Assess this cell for malaria.
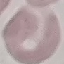

It is uninfected.

Summary:
  - Stain: Giemsa
  - Image type: automatically extracted cell patch, resized to 64 × 64 pixels
  - Capture: smartphone through the microscope eyepiece
  - Preparation: thin blood smear